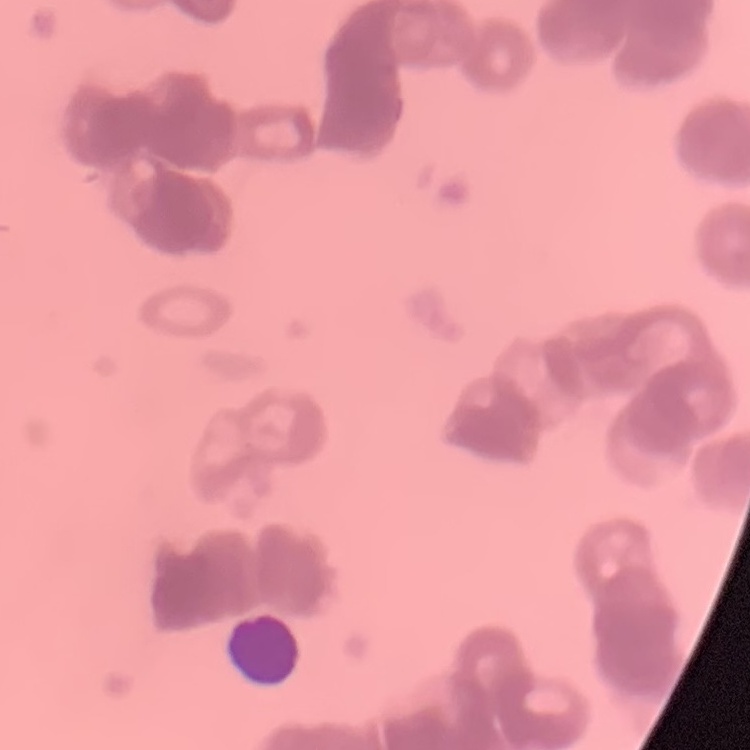
Summary:
  - Erythrocyte morphology: rouleaux formation
  - Stain: Field's or Giemsa
  - Preparation: thin peripheral smear
  - Image type: one tile cut from a larger photomicrograph